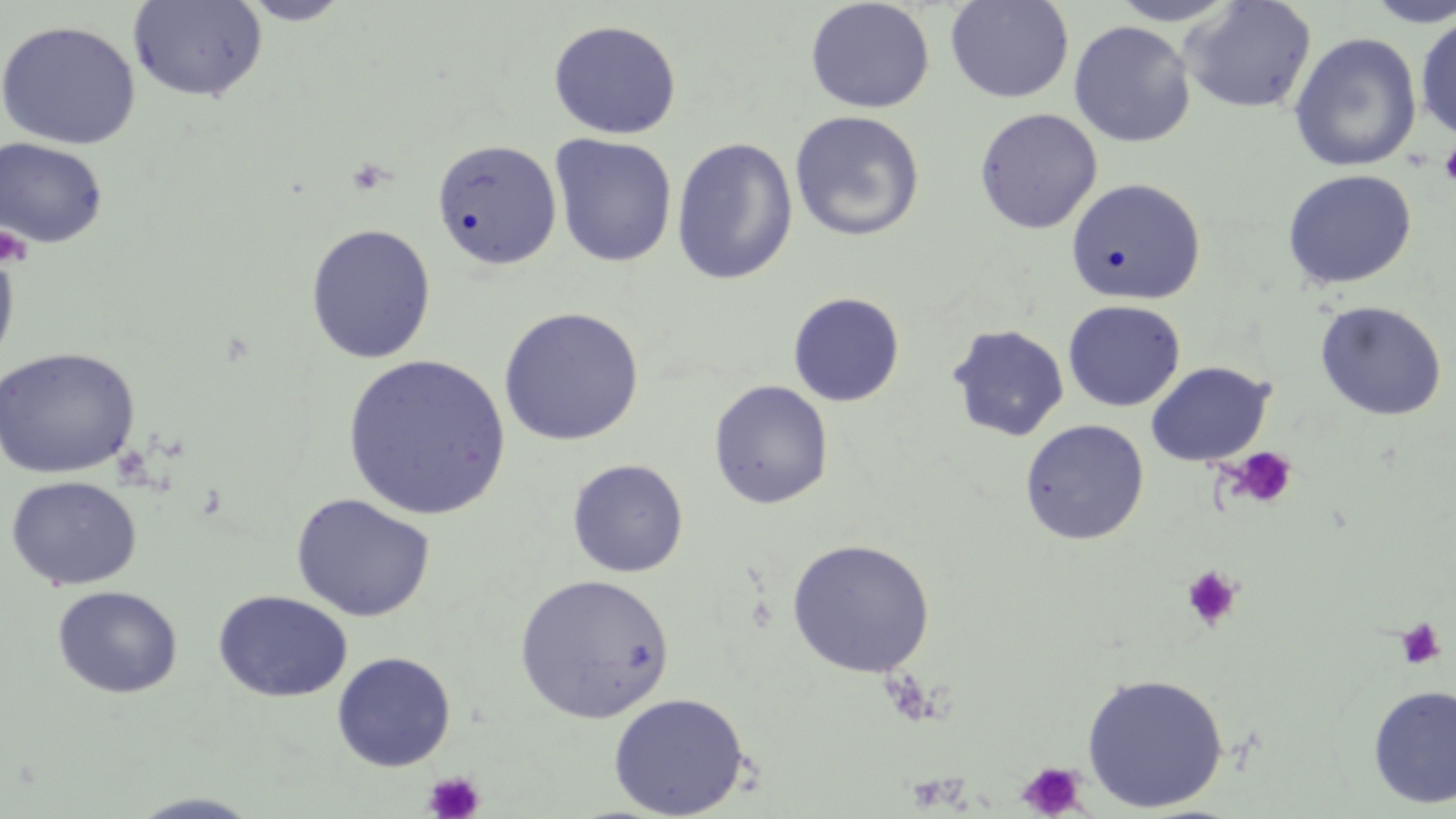
{
  "slide_level_diagnosis": "negative for blood parasites",
  "field_of_view": "one of a larger specimen",
  "magnification": "1000x",
  "preparation": "thin blood film",
  "platelet_locations": "approximate bounding boxes as named x1/y1/x2/y2 corners in pixels: (x1=1438, y1=142, x2=1456, y2=187), (x1=1, y1=224, x2=33, y2=268), (x1=1229, y1=447, x2=1297, y2=509), (x1=1181, y1=565, x2=1242, y2=630), (x1=1394, y1=617, x2=1447, y2=670), (x1=1016, y1=761, x2=1090, y2=819), (x1=423, y1=771, x2=485, y2=819)",
  "stain": "May-Grünwald-Giemsa",
  "modality": "optical microscopy",
  "image_size": "1456×819 pixels",
  "uninfected_red_blood_cell_locations": "approximate bounding boxes as named x1/y1/x2/y2 corners in pixels: (x1=236, y1=0, x2=355, y2=25), (x1=945, y1=0, x2=1074, y2=104), (x1=1107, y1=0, x2=1243, y2=26), (x1=1361, y1=0, x2=1456, y2=27), (x1=127, y1=1, x2=268, y2=103), (x1=804, y1=1, x2=935, y2=114), (x1=1181, y1=1, x2=1317, y2=114), (x1=1414, y1=13, x2=1456, y2=140), (x1=547, y1=19, x2=682, y2=139), (x1=0, y1=20, x2=141, y2=150), (x1=1068, y1=20, x2=1196, y2=148), (x1=1288, y1=32, x2=1423, y2=172), (x1=974, y1=108, x2=1103, y2=234), (x1=789, y1=110, x2=925, y2=241), (x1=549, y1=134, x2=677, y2=267), (x1=0, y1=137, x2=109, y2=248), (x1=671, y1=137, x2=798, y2=285), (x1=431, y1=139, x2=563, y2=271), (x1=1281, y1=169, x2=1417, y2=290), (x1=1066, y1=178, x2=1206, y2=305), (x1=305, y1=224, x2=436, y2=364), (x1=0, y1=242, x2=20, y2=377), (x1=788, y1=292, x2=905, y2=407), (x1=1063, y1=299, x2=1186, y2=412), (x1=1314, y1=300, x2=1448, y2=421), (x1=497, y1=306, x2=644, y2=446), (x1=947, y1=324, x2=1070, y2=442), (x1=0, y1=347, x2=140, y2=480), (x1=341, y1=354, x2=512, y2=521), (x1=1145, y1=361, x2=1275, y2=467), (x1=708, y1=379, x2=834, y2=509), (x1=1019, y1=419, x2=1149, y2=546), (x1=568, y1=459, x2=688, y2=577), (x1=5, y1=475, x2=142, y2=591), (x1=291, y1=493, x2=436, y2=623), (x1=785, y1=538, x2=935, y2=677), (x1=514, y1=573, x2=675, y2=723), (x1=52, y1=585, x2=182, y2=699), (x1=213, y1=590, x2=353, y2=702), (x1=332, y1=652, x2=456, y2=771), (x1=1081, y1=672, x2=1228, y2=812), (x1=1368, y1=684, x2=1456, y2=809), (x1=607, y1=692, x2=749, y2=819), (x1=125, y1=792, x2=266, y2=818)"
}